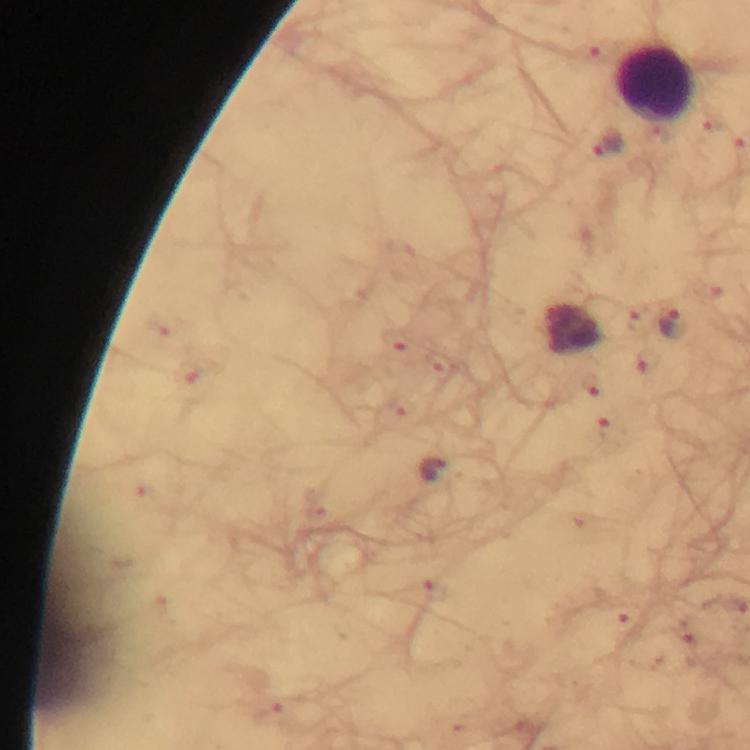
Approximate centers as {x, y} in pixels.
Summary:
  - Plasmodium parasite locations: {607, 144}, {674, 323}, {433, 469}
  - Leukocyte locations: {656, 82}
  - Stain: Giemsa
  - Context: from a diagnostic examination for malaria
  - Immersion oil: applied
  - Image size: 750×750 pixels
  - Magnification: 100x
  - Preparation: thick smear
  - Capture: smartphone photograph through a microscope
  - Cropped from: one field of view